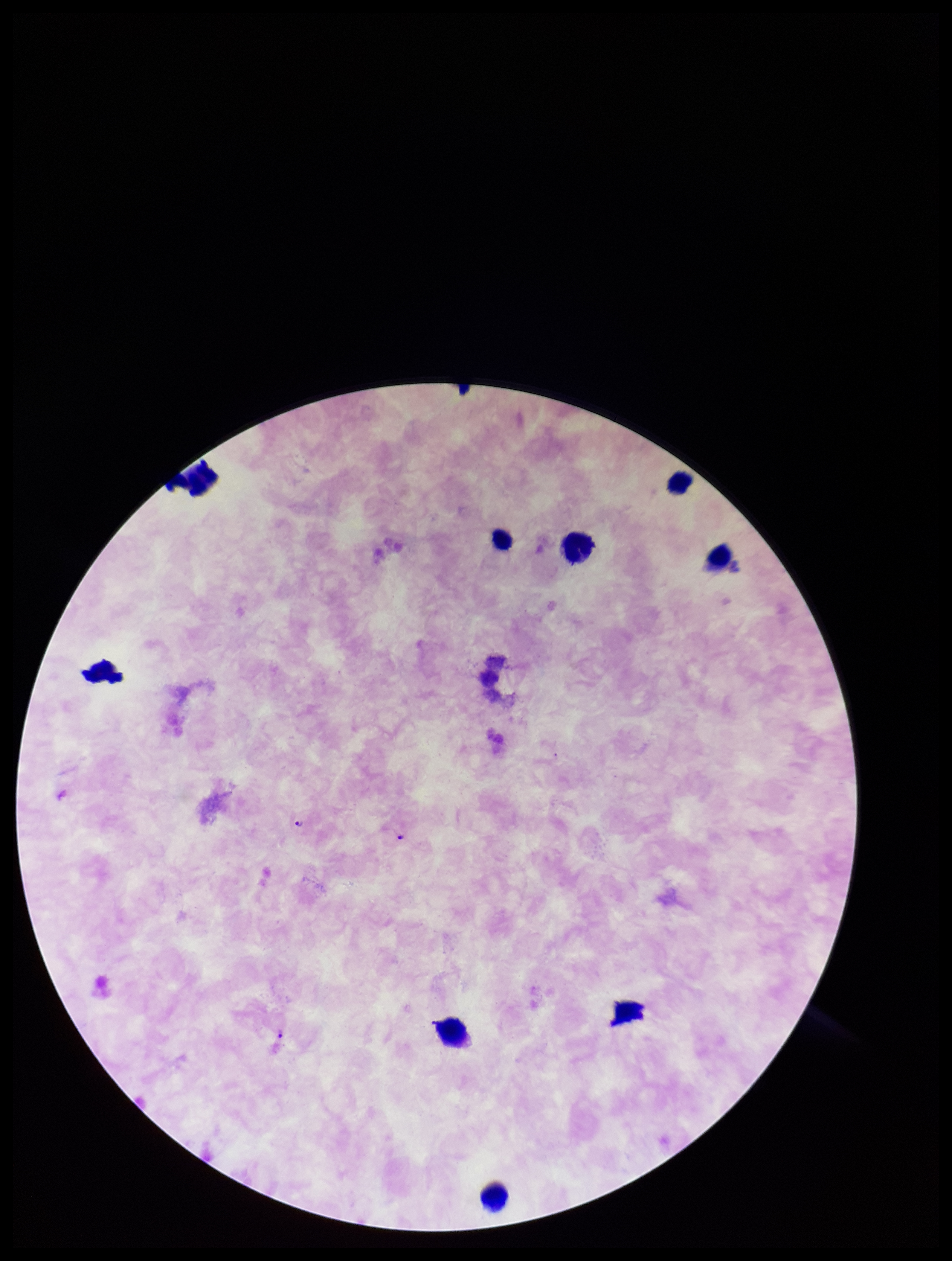 Plasmodium parasites: seen. Leukocyte count: 9. Patient malaria status: infected. Preparation: thick. Species reported for this patient: Plasmodium falciparum. Parasite count: 2. Giemsa stain. Single field of view. Image is 952×1261 pixels. Smartphone photograph taken through the eyepiece of a microscope.